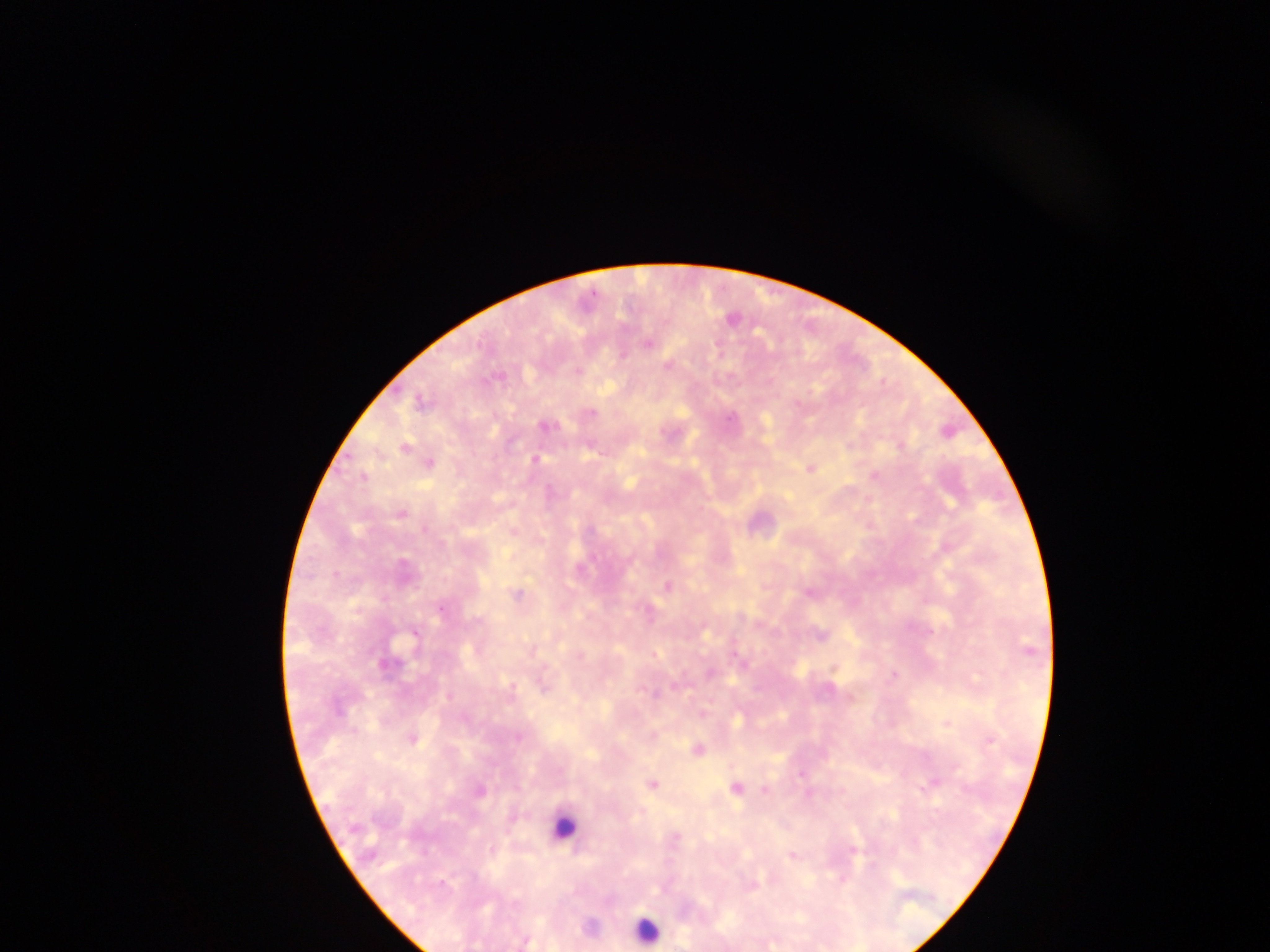
Approximate centers as (x, y) in pixels.
Summary:
  - Plasmodium parasite locations: (647, 344), (623, 354), (591, 413), (546, 427), (535, 459), (400, 513), (669, 585), (809, 591), (518, 594), (442, 609), (819, 634), (532, 650), (832, 668), (893, 675), (674, 683), (656, 695), (448, 697), (850, 697), (520, 736), (991, 741), (696, 750), (800, 776), (652, 783), (736, 788), (764, 790), (675, 838), (852, 853), (790, 855), (527, 941)
  - Leukocyte locations: (567, 825), (644, 925)
  - Image size: 1270×952 pixels
  - Capture: mobile-phone photograph through a microscope
  - Preparation: thick blood smear
  - Field of view: single
  - Country: Ghana